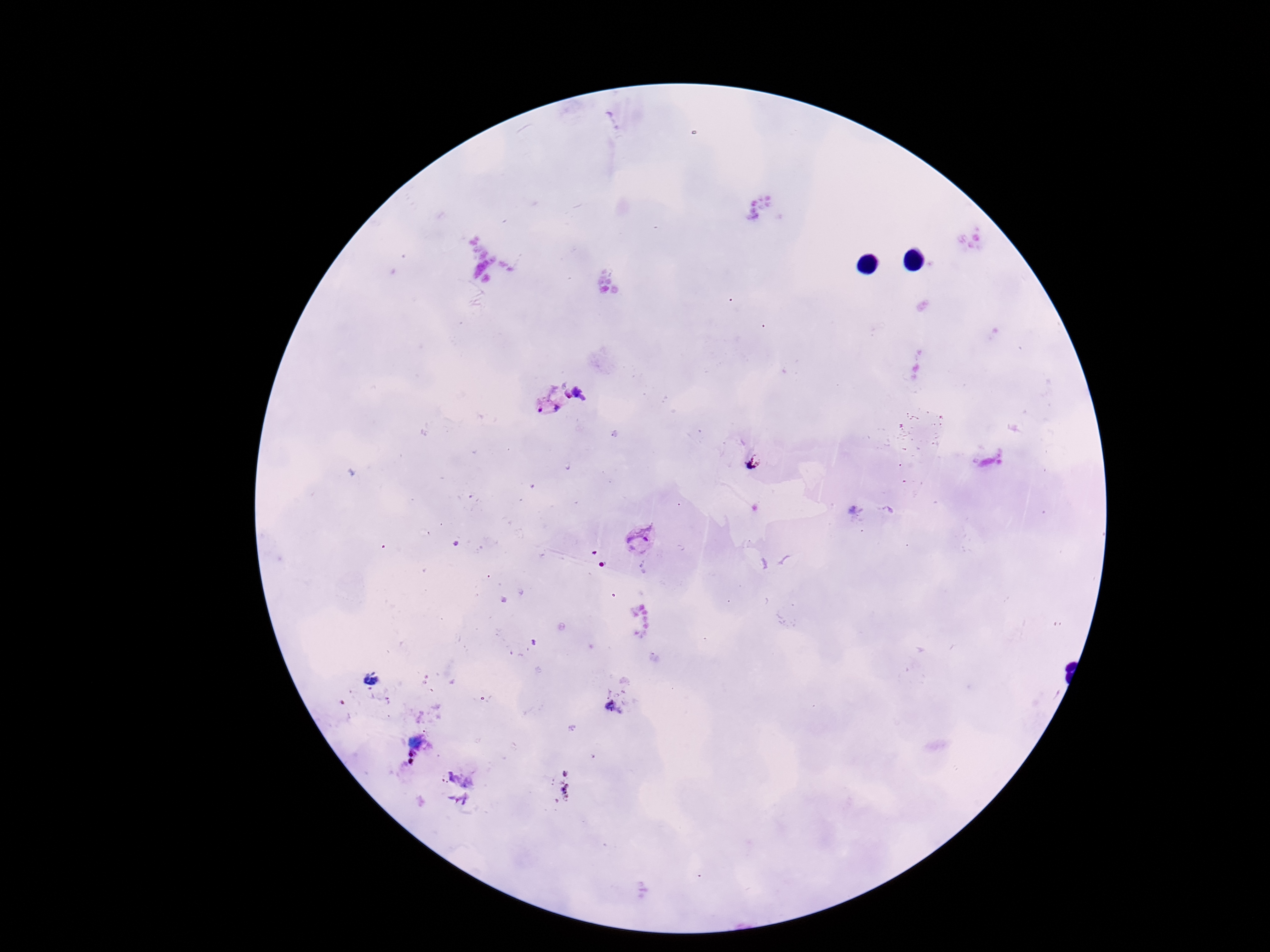

Approximate centers as [x, y] in pixels. Plasmodium parasite locations: [551, 403], [639, 541]. Image is 1270×952 pixels. Smartphone photograph taken through the microscope eyepiece. Thick blood smear. Single field of view. Patient malaria status: positive. 100x magnification. Giemsa-stained preparation.